Locate every blood parasite and identify its species.
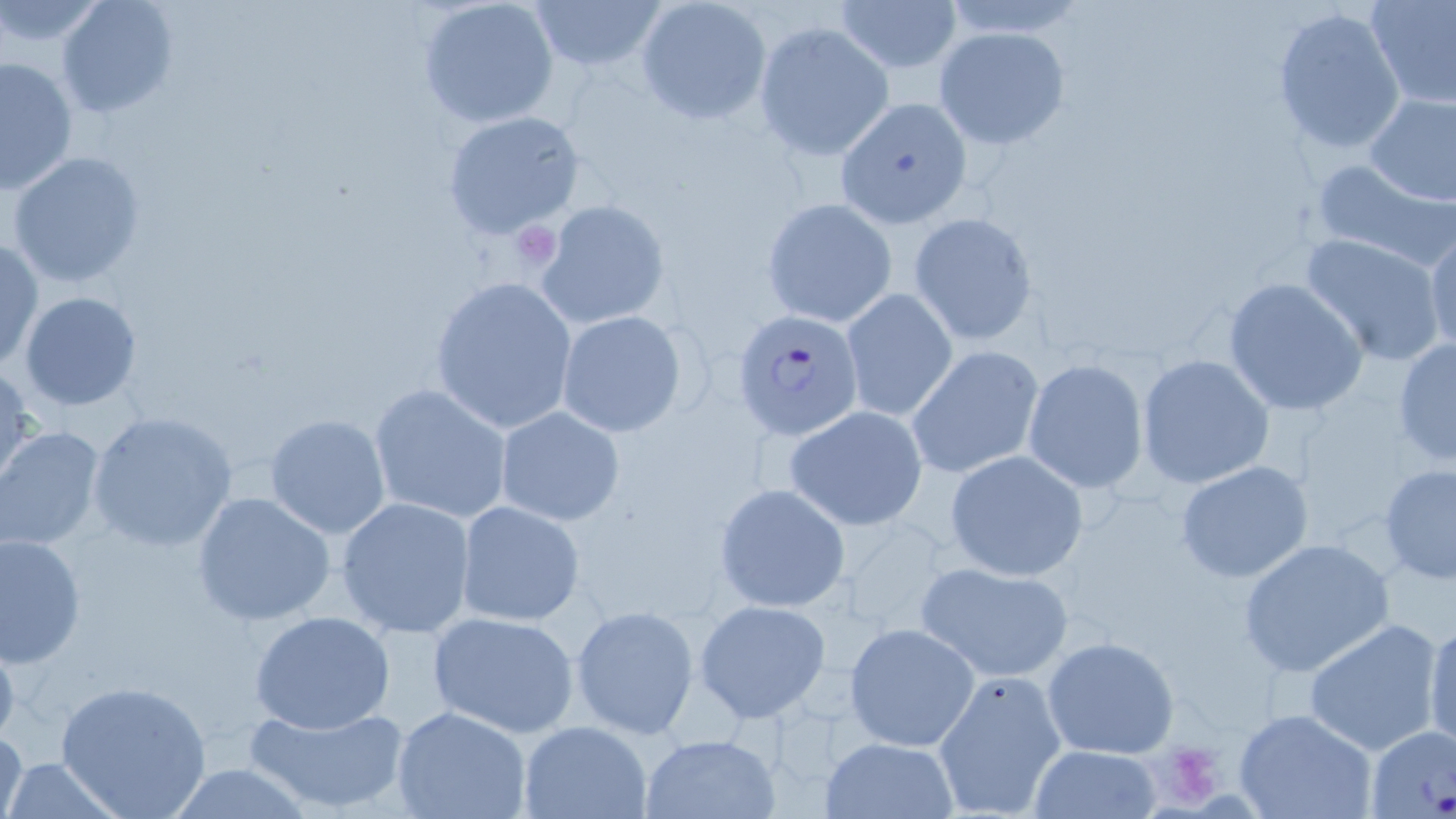
Approximate bounding boxes as [x1, y1, x2, y2] in pixels.
Plasmodium falciparum-infected red blood cells: [731, 310, 863, 442].
No Plasmodium ovale, Plasmodium malariae, Plasmodium vivax, Babesia divergens, or Trypanosoma brucei observed.

{
  "slide_level_diagnosis": "Plasmodium falciparum",
  "stain": "May-Grünwald-Giemsa",
  "image_size": "1456×819 pixels",
  "modality": "optical microscopy",
  "preparation": "thin blood film",
  "magnification": "1000x",
  "uninfected_red_blood_cell_locations": "approximate bounding boxes as [x1, y1, x2, y2] in pixels: [0, 0, 108, 48], [55, 0, 179, 118], [418, 0, 560, 130], [526, 0, 669, 75], [835, 0, 962, 75], [1364, 0, 1456, 108], [634, 1, 771, 124], [1271, 7, 1408, 157], [754, 21, 894, 160], [935, 26, 1070, 148], [0, 55, 78, 195], [1363, 90, 1456, 206], [834, 96, 971, 229], [440, 109, 587, 240], [6, 150, 147, 289], [1310, 157, 1456, 272], [761, 198, 898, 329], [536, 200, 671, 329], [907, 211, 1039, 347], [1424, 227, 1456, 360], [1300, 232, 1447, 365], [0, 238, 43, 371], [429, 275, 578, 435], [1222, 277, 1370, 418], [842, 290, 959, 421], [18, 291, 144, 410], [555, 309, 689, 436], [1392, 337, 1456, 468], [907, 346, 1044, 479], [1136, 354, 1276, 490], [1022, 359, 1148, 493], [0, 363, 36, 493], [368, 383, 516, 524], [494, 405, 624, 527], [784, 405, 929, 531], [85, 411, 240, 553], [264, 413, 392, 539], [0, 427, 107, 552], [943, 450, 1088, 578], [1175, 459, 1314, 584], [1376, 464, 1456, 586], [714, 484, 851, 612], [192, 491, 337, 628], [335, 496, 478, 638], [454, 500, 586, 628], [1, 533, 86, 666], [1237, 538, 1395, 677], [915, 560, 1075, 682], [693, 599, 832, 721], [570, 605, 700, 738], [248, 609, 399, 735], [426, 610, 582, 740], [1423, 613, 1456, 755], [1302, 619, 1445, 756], [845, 623, 978, 751], [0, 628, 22, 756], [1042, 636, 1180, 759], [934, 670, 1066, 816], [56, 677, 212, 819], [243, 700, 413, 816], [391, 706, 533, 818], [1232, 709, 1379, 819], [517, 719, 655, 819], [1364, 725, 1456, 817], [0, 726, 27, 819], [641, 732, 778, 817], [820, 737, 956, 816], [1027, 744, 1165, 819], [0, 757, 125, 817], [158, 763, 320, 819]",
  "platelet_locations": "approximate bounding boxes as [x1, y1, x2, y2] in pixels: [507, 221, 559, 269], [1160, 743, 1220, 807]",
  "field_of_view": "one of a larger specimen"
}